Assess the morphology of the red blood cells.
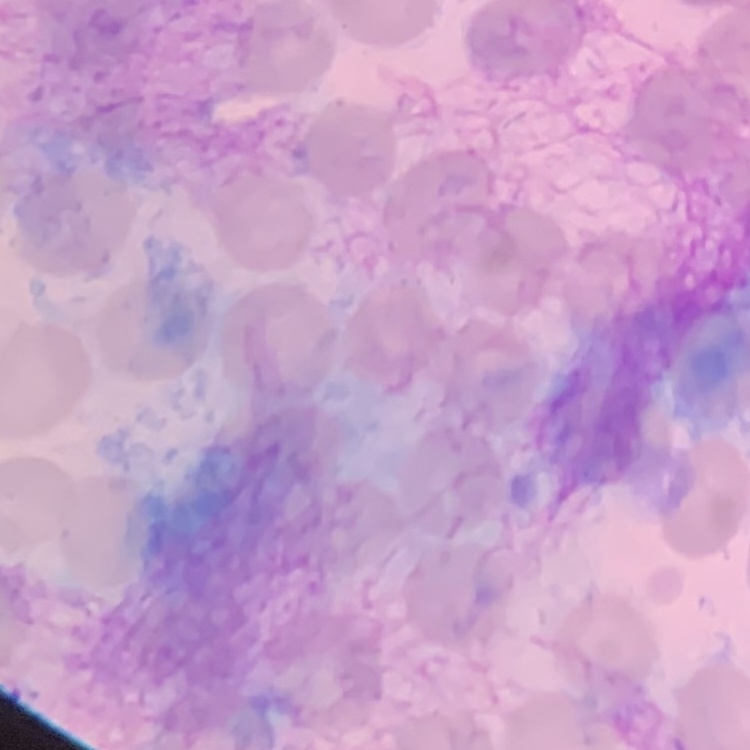
They show no rouleaux formation.

Thin blood smear. Square crop of a larger photomicrograph. Stained with either Field's or Giemsa.